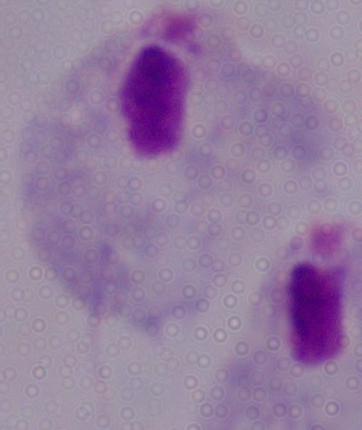

A trichomonad is seen. Micrograph. Captured at 1000x magnification.